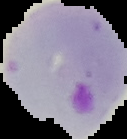

preparation = thin blood smear
result = malaria parasites identified
image size = 127×139 pixels
image type = segmented cell region with the area outside set to black